State which parasite is depicted.
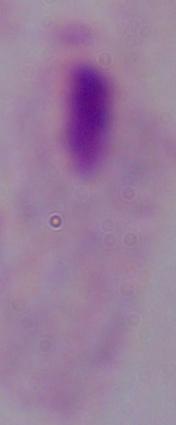
A trichomonad.

modality = micrograph
magnification = 1000x